Report the malaria status.
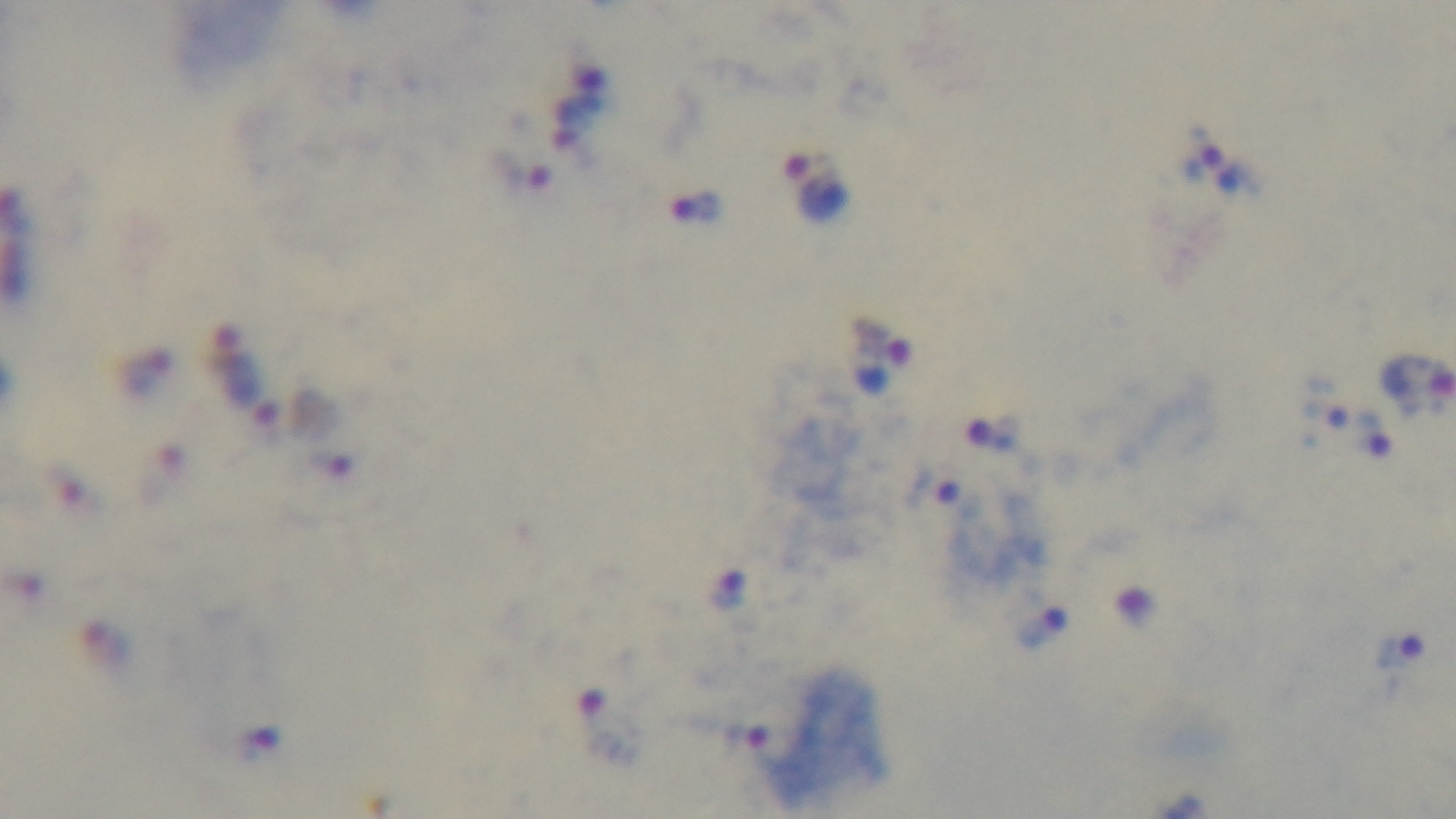
Positive.

Photomicrograph. Giemsa-stained. Captured with a mounted 4K digital camera. 100x oil-immersion objective. Preparation: thick blood film. Single field of view.